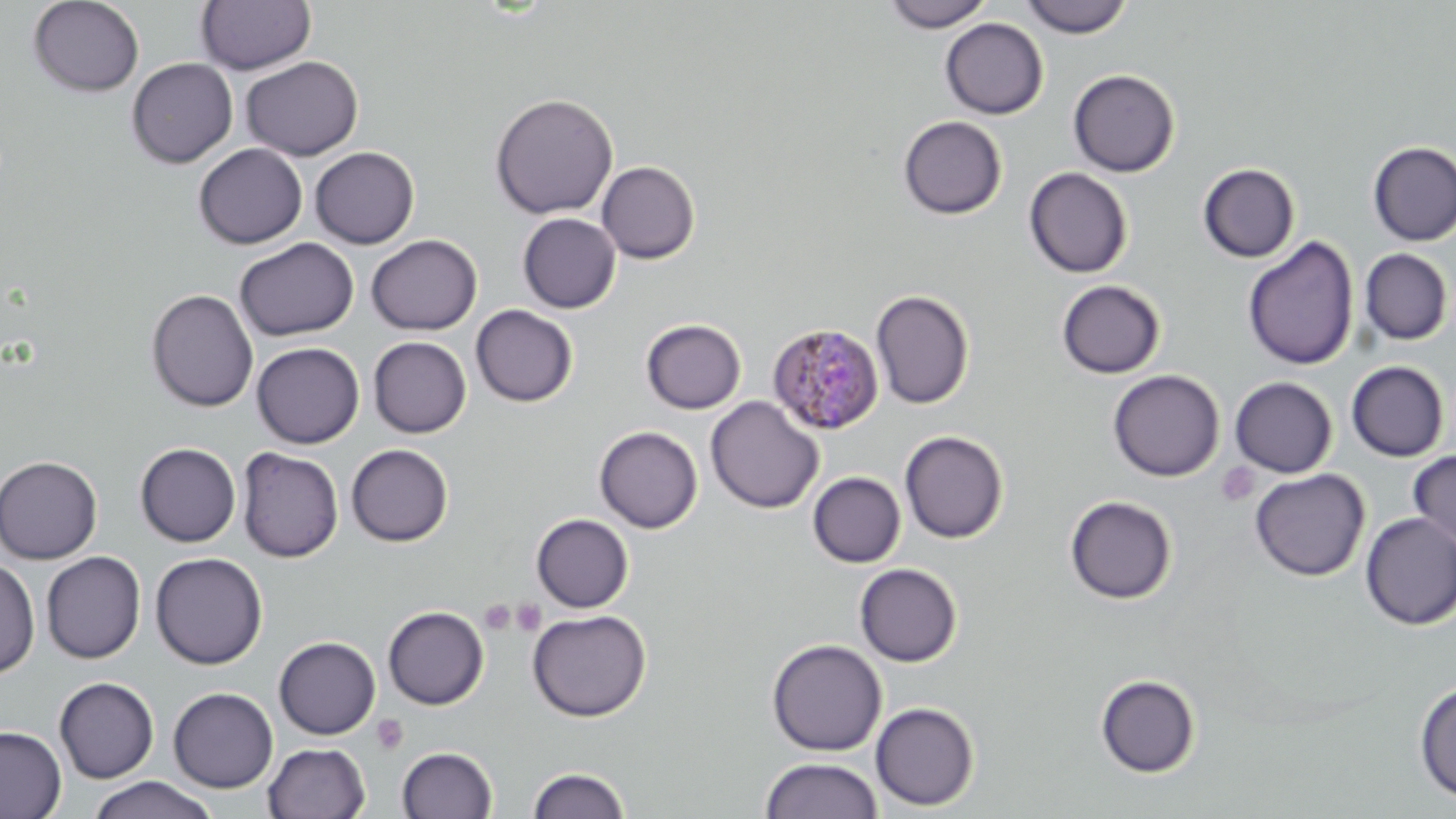

Approximate bounding boxes as named x1/y1/x2/y2 corners in pixels. Uninfected red blood cell locations: (x1=28, y1=0, x2=144, y2=96), (x1=196, y1=0, x2=316, y2=74), (x1=883, y1=0, x2=995, y2=31), (x1=1019, y1=0, x2=1133, y2=38), (x1=940, y1=18, x2=1048, y2=119), (x1=241, y1=55, x2=364, y2=160), (x1=126, y1=57, x2=238, y2=168), (x1=1068, y1=69, x2=1180, y2=177), (x1=489, y1=93, x2=618, y2=219), (x1=898, y1=115, x2=1007, y2=220), (x1=1368, y1=141, x2=1456, y2=246), (x1=194, y1=143, x2=307, y2=249), (x1=310, y1=146, x2=419, y2=249), (x1=596, y1=161, x2=700, y2=264), (x1=1197, y1=163, x2=1300, y2=263), (x1=1023, y1=166, x2=1133, y2=278), (x1=517, y1=213, x2=621, y2=313), (x1=366, y1=234, x2=482, y2=335), (x1=1242, y1=236, x2=1359, y2=370), (x1=234, y1=237, x2=359, y2=341), (x1=1359, y1=248, x2=1453, y2=345), (x1=1055, y1=279, x2=1166, y2=379), (x1=146, y1=288, x2=259, y2=413), (x1=871, y1=289, x2=974, y2=409), (x1=470, y1=304, x2=578, y2=407), (x1=641, y1=319, x2=746, y2=414), (x1=368, y1=337, x2=471, y2=438), (x1=251, y1=342, x2=364, y2=448), (x1=1345, y1=361, x2=1449, y2=462), (x1=1107, y1=369, x2=1225, y2=481), (x1=1229, y1=376, x2=1338, y2=478), (x1=705, y1=396, x2=824, y2=514), (x1=594, y1=426, x2=703, y2=532), (x1=899, y1=430, x2=1008, y2=543), (x1=135, y1=443, x2=241, y2=547), (x1=346, y1=444, x2=454, y2=546), (x1=236, y1=448, x2=343, y2=562), (x1=1408, y1=449, x2=1456, y2=550), (x1=0, y1=455, x2=103, y2=564), (x1=1249, y1=468, x2=1370, y2=581), (x1=807, y1=471, x2=906, y2=568), (x1=1064, y1=494, x2=1178, y2=604), (x1=531, y1=513, x2=634, y2=612), (x1=1359, y1=513, x2=1456, y2=631), (x1=41, y1=552, x2=146, y2=663), (x1=150, y1=552, x2=268, y2=669), (x1=0, y1=556, x2=40, y2=680), (x1=854, y1=563, x2=962, y2=667), (x1=382, y1=606, x2=489, y2=710), (x1=527, y1=609, x2=651, y2=722), (x1=273, y1=636, x2=380, y2=739), (x1=766, y1=639, x2=887, y2=756), (x1=1095, y1=673, x2=1200, y2=778), (x1=54, y1=676, x2=159, y2=783), (x1=1413, y1=681, x2=1456, y2=804), (x1=168, y1=687, x2=278, y2=792), (x1=870, y1=701, x2=980, y2=811), (x1=0, y1=725, x2=66, y2=819), (x1=263, y1=742, x2=370, y2=818), (x1=397, y1=746, x2=497, y2=819), (x1=759, y1=756, x2=884, y2=819), (x1=527, y1=766, x2=631, y2=818), (x1=87, y1=777, x2=218, y2=819). Plasmodium malariae-infected red blood cell locations: (x1=767, y1=322, x2=884, y2=436). Platelet locations: (x1=1217, y1=463, x2=1260, y2=507), (x1=511, y1=599, x2=547, y2=636), (x1=479, y1=600, x2=517, y2=636), (x1=371, y1=714, x2=409, y2=755). Slide-level diagnosis: Plasmodium malariae. Image is 1456×819 pixels. Captured at 1000x magnification. One field of a larger specimen. May-Grünwald-Giemsa-stained preparation. Thin blood smear. Light microscopy.